Locate every Plasmodium parasite.
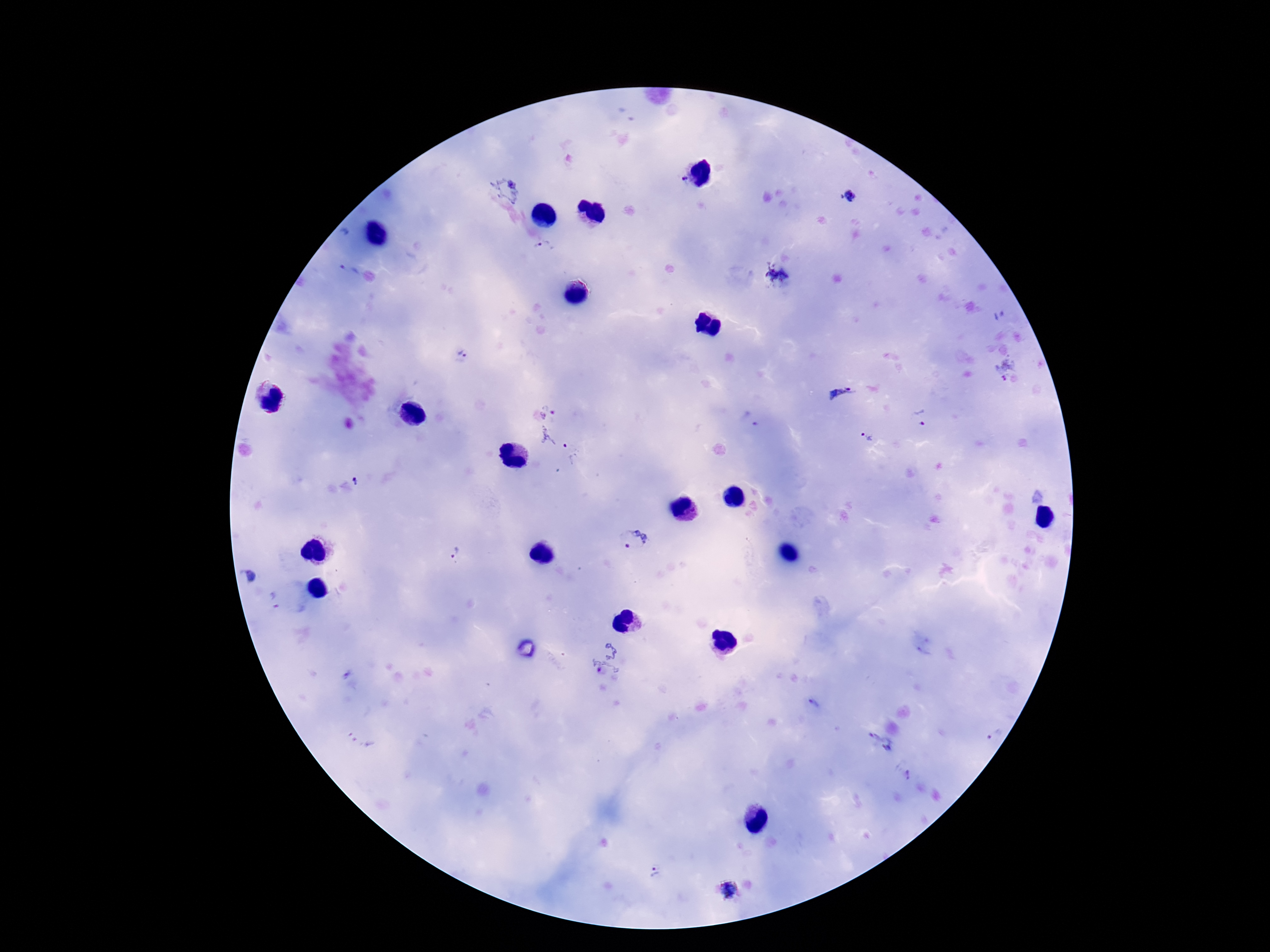
Approximate object centers, in pixels from the top-left corner.
Plasmodium parasites: (x=684, y=180), (x=508, y=189), (x=848, y=196), (x=544, y=248), (x=351, y=270), (x=778, y=276), (x=462, y=354), (x=1006, y=368), (x=841, y=393), (x=548, y=413), (x=921, y=418), (x=749, y=419), (x=866, y=438), (x=554, y=442), (x=355, y=482), (x=632, y=541), (x=453, y=552), (x=249, y=577), (x=275, y=601), (x=608, y=658), (x=814, y=704), (x=361, y=736), (x=995, y=736), (x=880, y=745), (x=906, y=775), (x=654, y=873), (x=729, y=892).

Thick blood film. Smartphone photograph taken through the microscope eyepiece. 100x magnification. One field from this slide. Patient malaria status: positive. Giemsa-stained preparation. Image is 1270×952 pixels.